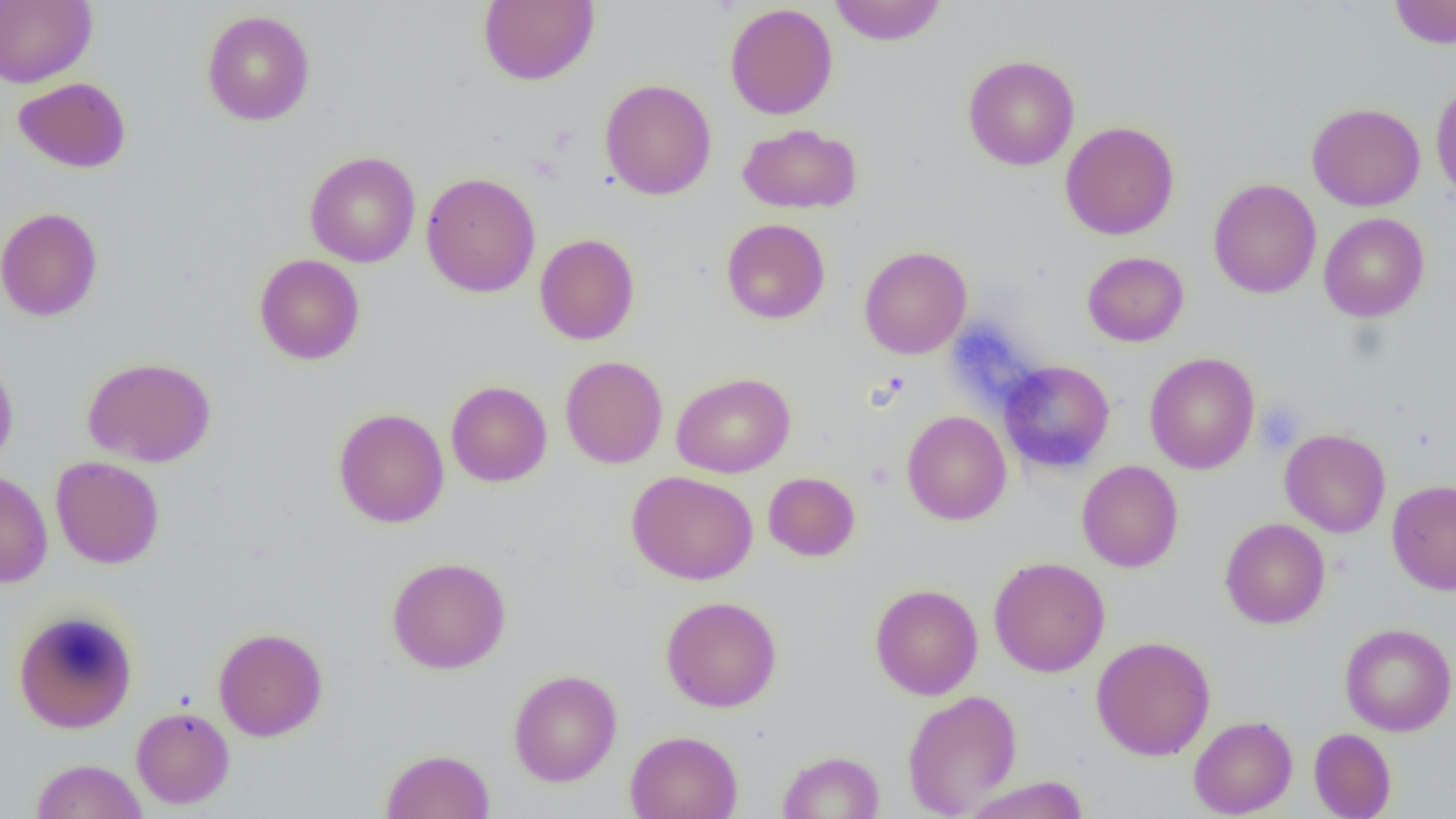

Summary:
  - Coordinate format: approximate bounding boxes as [x1, y1, x2, y2] in pixels
  - Uninfected red blood cell locations: [478, 0, 599, 86], [829, 0, 947, 46], [1389, 0, 1456, 49], [0, 1, 96, 88], [724, 3, 838, 120], [201, 10, 315, 126], [962, 54, 1079, 171], [13, 77, 131, 173], [599, 79, 717, 200], [1431, 79, 1456, 205], [1306, 102, 1425, 211], [1060, 121, 1179, 240], [738, 123, 862, 214], [305, 151, 420, 268], [421, 172, 541, 297], [1208, 178, 1322, 298], [1, 207, 103, 322], [1318, 213, 1430, 322], [721, 218, 830, 324], [535, 233, 640, 345], [859, 246, 972, 359], [1082, 251, 1189, 347], [254, 254, 365, 365], [1144, 352, 1260, 474], [0, 356, 18, 471], [82, 356, 217, 467], [560, 356, 668, 469], [999, 360, 1115, 473], [671, 372, 796, 478], [445, 377, 669, 477], [446, 381, 552, 487], [333, 407, 449, 528], [901, 410, 1012, 525], [1280, 428, 1390, 538], [50, 455, 164, 569], [1077, 461, 1183, 572], [0, 469, 53, 588], [627, 470, 758, 585], [763, 471, 860, 561], [1387, 479, 1456, 594], [1220, 517, 1330, 629], [387, 556, 511, 674], [989, 557, 1110, 677], [870, 583, 983, 700], [661, 595, 782, 713], [13, 608, 138, 733], [1339, 622, 1456, 736], [213, 626, 328, 742], [1091, 636, 1216, 760], [508, 669, 622, 787], [902, 690, 1022, 817], [131, 706, 234, 809], [1188, 715, 1298, 818], [1309, 728, 1396, 818], [625, 730, 742, 819], [380, 748, 496, 819], [778, 751, 885, 818], [30, 759, 148, 819], [964, 776, 1090, 819]
  - Platelet locations: [1255, 400, 1307, 456]
  - Slide-level diagnosis: no evidence of blood parasites
  - Field of view: single
  - Modality: light microscopy
  - Image size: 1456×819 pixels
  - Preparation: thin blood smear
  - Magnification: 1000x